Describe the morphology of the red blood cells.
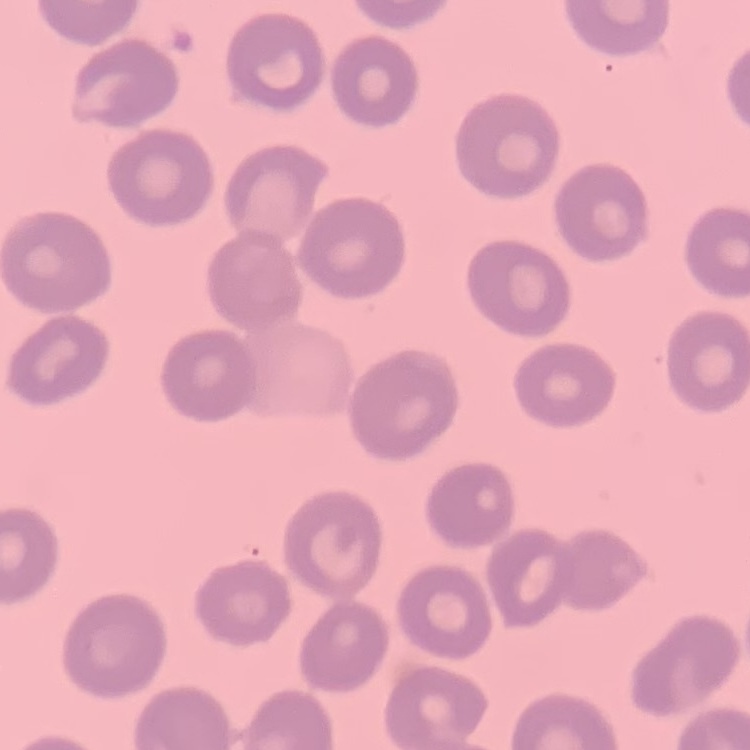

No rouleaux formation.

Summary:
  - Image type: one tile cut from a larger photomicrograph
  - Stain: Field's or Giemsa
  - Preparation: thin peripheral smear